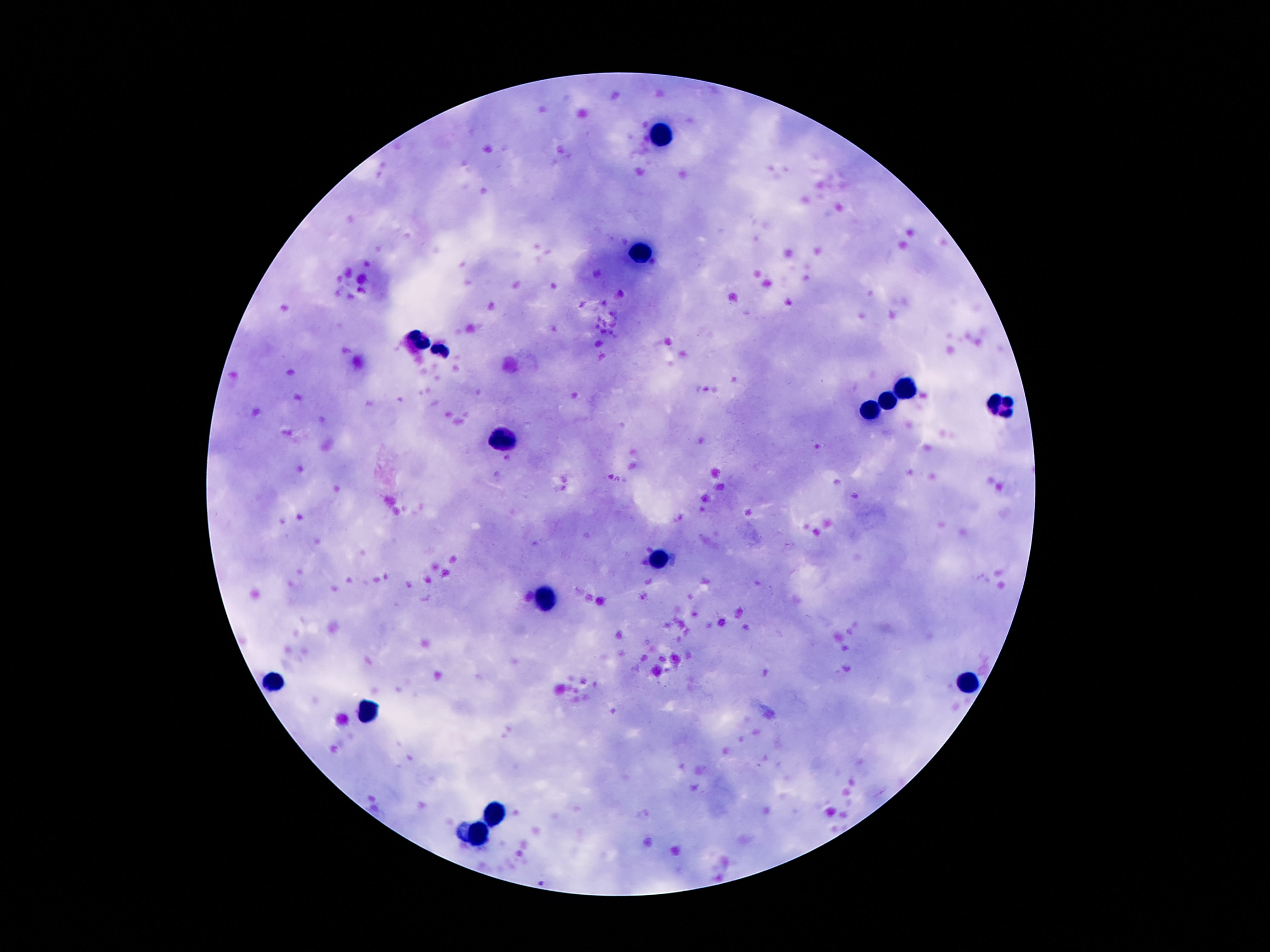 Approximate centers as {x, y} in pixels. Leukocyte locations: {658, 135}, {641, 252}, {413, 338}, {444, 347}, {904, 382}, {888, 400}, {1003, 407}, {871, 413}, {501, 440}, {658, 559}, {546, 599}, {276, 682}, {968, 684}, {366, 710}, {495, 816}, {477, 836}. Giemsa-stained preparation. Patient malaria status: uninfected. 100x magnification. Photographed through the microscope eyepiece with a smartphone camera. Thick blood film. Image is 1270×952 pixels. One field from this slide.